Assess this cell for malaria.
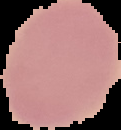

Uninfected.

preparation: thin blood film
image_size: 121×130 pixels
image_type: cell region segmented out of the field of view; surrounding area masked to black